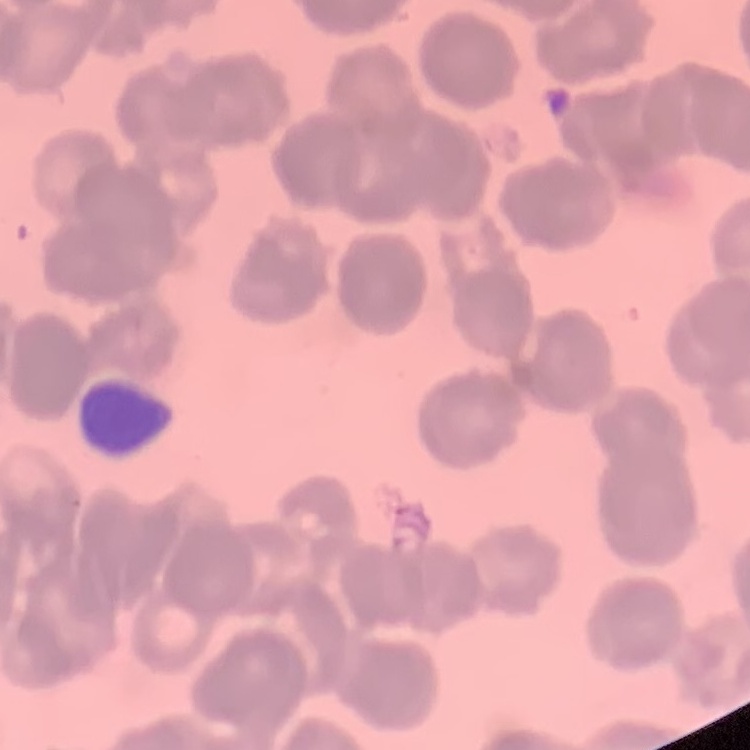
erythrocyte morphology = rouleaux formation
stain = Field's or Giemsa
image type = one tile cut from a larger photomicrograph
preparation = thin blood film